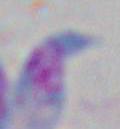

modality: micrograph
magnification: 1000x
identification: Toxoplasma gondii